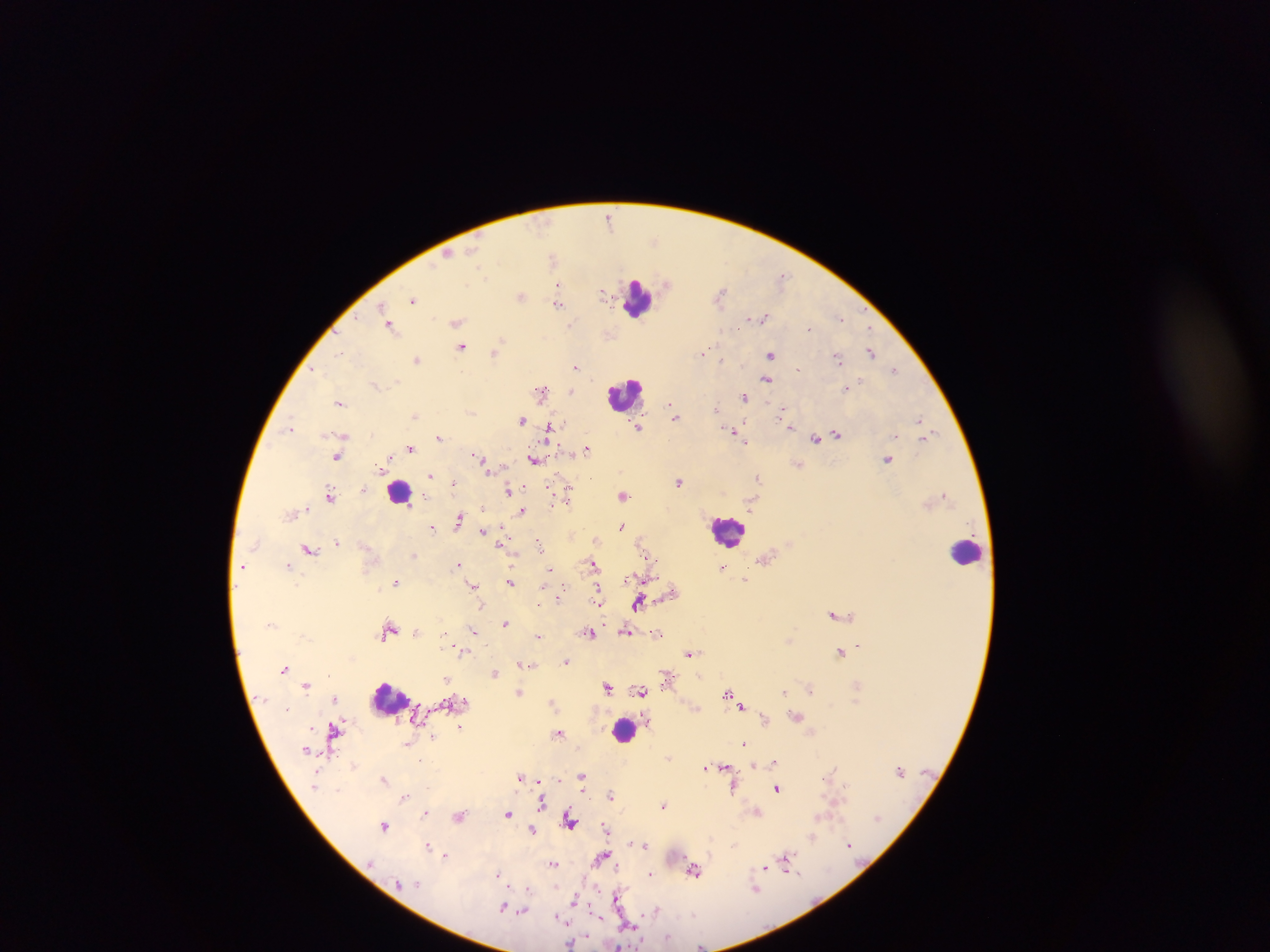
Approximate centers as (x, y) in pixels.
Summary:
  - Plasmodium parasite locations: (608, 213), (608, 220), (450, 254), (552, 258), (782, 274), (558, 283), (720, 290), (604, 293), (413, 299), (384, 305), (559, 305), (841, 315), (765, 317), (457, 322), (809, 327), (868, 329), (463, 345), (704, 349), (871, 352), (703, 353), (341, 354), (771, 354), (837, 356), (418, 360), (721, 360), (894, 367), (577, 368), (767, 378), (375, 384), (571, 390), (542, 391), (744, 397), (339, 404), (717, 408), (781, 411), (675, 416), (417, 417), (521, 419), (919, 419), (789, 425), (640, 428), (288, 431), (733, 432), (837, 434), (344, 436), (922, 436), (439, 437), (895, 437), (744, 438), (816, 438), (747, 441), (411, 449), (587, 449), (389, 456), (477, 456), (337, 457), (480, 459), (535, 459), (888, 460), (378, 468), (432, 474), (758, 478), (678, 482), (454, 483), (567, 487), (510, 490), (566, 493), (329, 495), (623, 496), (944, 496), (483, 508), (521, 512), (459, 517), (623, 527), (433, 528), (483, 531), (504, 532), (336, 542), (503, 544), (539, 544), (309, 549), (593, 563), (290, 565), (456, 565), (548, 568), (723, 568), (512, 581), (397, 582), (473, 585), (597, 594), (561, 595), (560, 599), (638, 603), (481, 605), (599, 606), (834, 614), (505, 622), (474, 629), (416, 631), (627, 631), (445, 632), (591, 632), (657, 633), (538, 637), (790, 637), (860, 644), (841, 653), (691, 655), (566, 662), (523, 664), (531, 664), (285, 669), (497, 672), (699, 676), (446, 680), (306, 684), (809, 688), (519, 691), (784, 691), (726, 693), (333, 697), (553, 704), (742, 706), (463, 725), (560, 734), (430, 737), (743, 743), (418, 760), (757, 764), (708, 765), (724, 766), (703, 768), (728, 768), (583, 774), (519, 775), (558, 779), (384, 780), (734, 785), (426, 788), (777, 788), (611, 794), (403, 798), (543, 801), (663, 804), (424, 813), (508, 813), (757, 813), (459, 816), (875, 817), (605, 828), (533, 829), (385, 830), (814, 837), (631, 841), (849, 844), (428, 845), (645, 846), (446, 854), (602, 858), (786, 858), (553, 863), (615, 868), (765, 868), (786, 868), (496, 875), (648, 875), (529, 889), (757, 890), (618, 897), (575, 899), (502, 908), (654, 909), (524, 911), (597, 916), (558, 919), (628, 925), (569, 943), (619, 944), (700, 945)
  - Leukocyte locations: (639, 300), (626, 396), (399, 490), (730, 529), (964, 549), (393, 699), (619, 723)
  - Image size: 1270×952 pixels
  - Field of view: single
  - Preparation: thick blood smear
  - Country: Ghana
  - Capture: mobile-phone photograph through a microscope